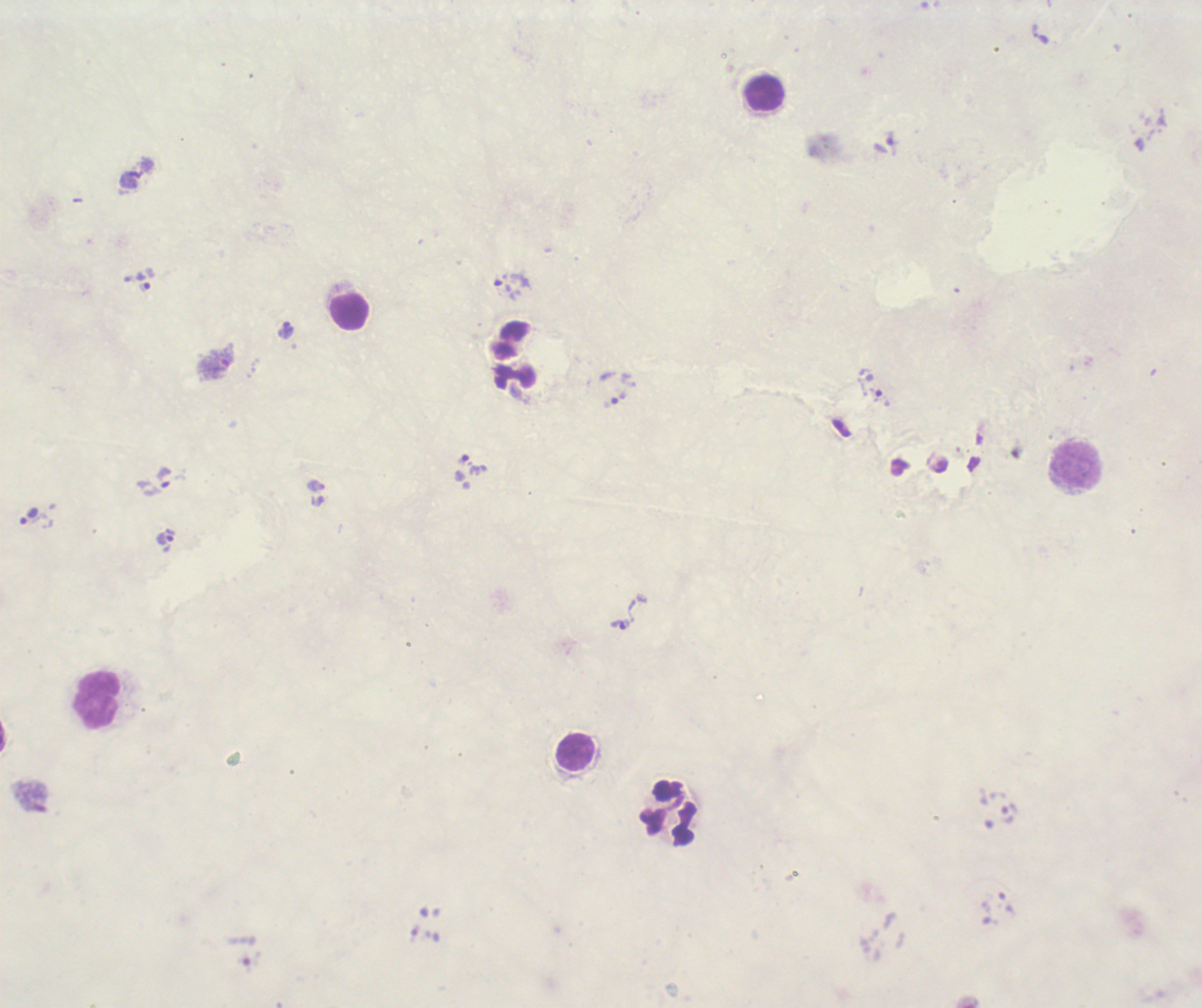

image_size: 1202×1008 pixels
result: positive for Plasmodium parasites
stain: Romanowsky
trophozoite_locations: 'approximate centers as {x, y} in pixels: {892, 138}, {144, 282}, {503, 282}, {286, 330}, {215, 364}, {882, 398}, {619, 399}, {473, 465}, {163, 478}, {316, 486}, {29, 516}, {165, 539}, {620, 625}'
coloration_quality: bad
leukocyte_locations: 'approximate centers as {x, y} in pixels: {765, 94}, {349, 313}, {1076, 464}, {98, 700}, {576, 752}, {668, 814}'
magnification: 100x
field_of_view: single
context: previously used in a real diagnosis
background_quality: unsatisfactory
preparation: thick blood smear